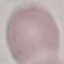

Malaria status: uninfected. Thin blood smear. Giemsa stain. Automatically extracted cell patch, resized to 64 × 64 pixels. Photographed with a smartphone camera at the microscope eyepiece.